Assess the morphology of the erythrocytes.
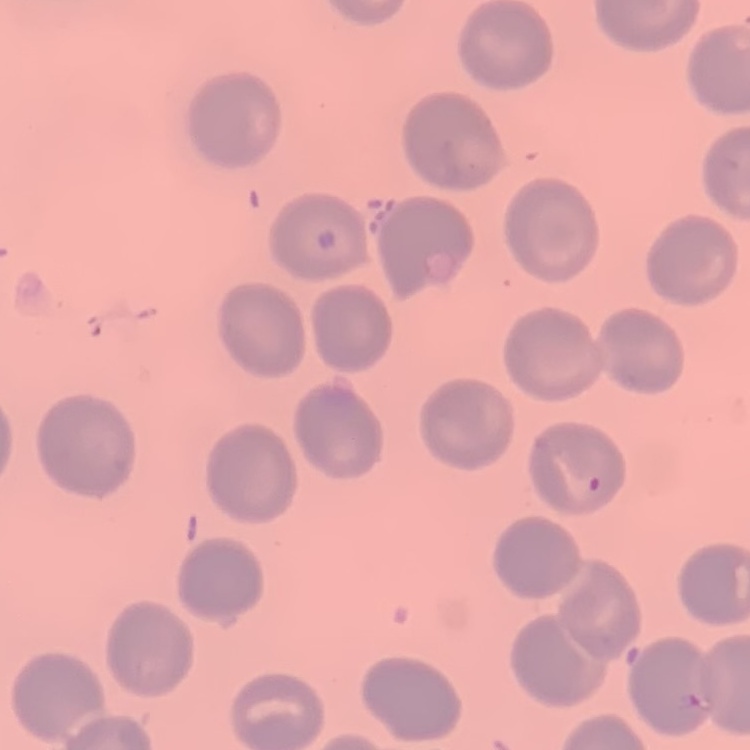
They show no rouleaux formation.

Thin blood smear. Stained with either Field's or Giemsa. Square crop of a larger photomicrograph.